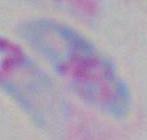
Toxoplasma gondii is seen. Micrograph. Captured at 1000x magnification.